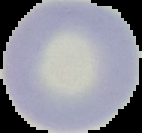

Summary:
  - Result: no Plasmodium parasites detected
  - Image size: 142×133 pixels
  - Image type: segmented cell region with the area outside set to black
  - Preparation: thin blood smear